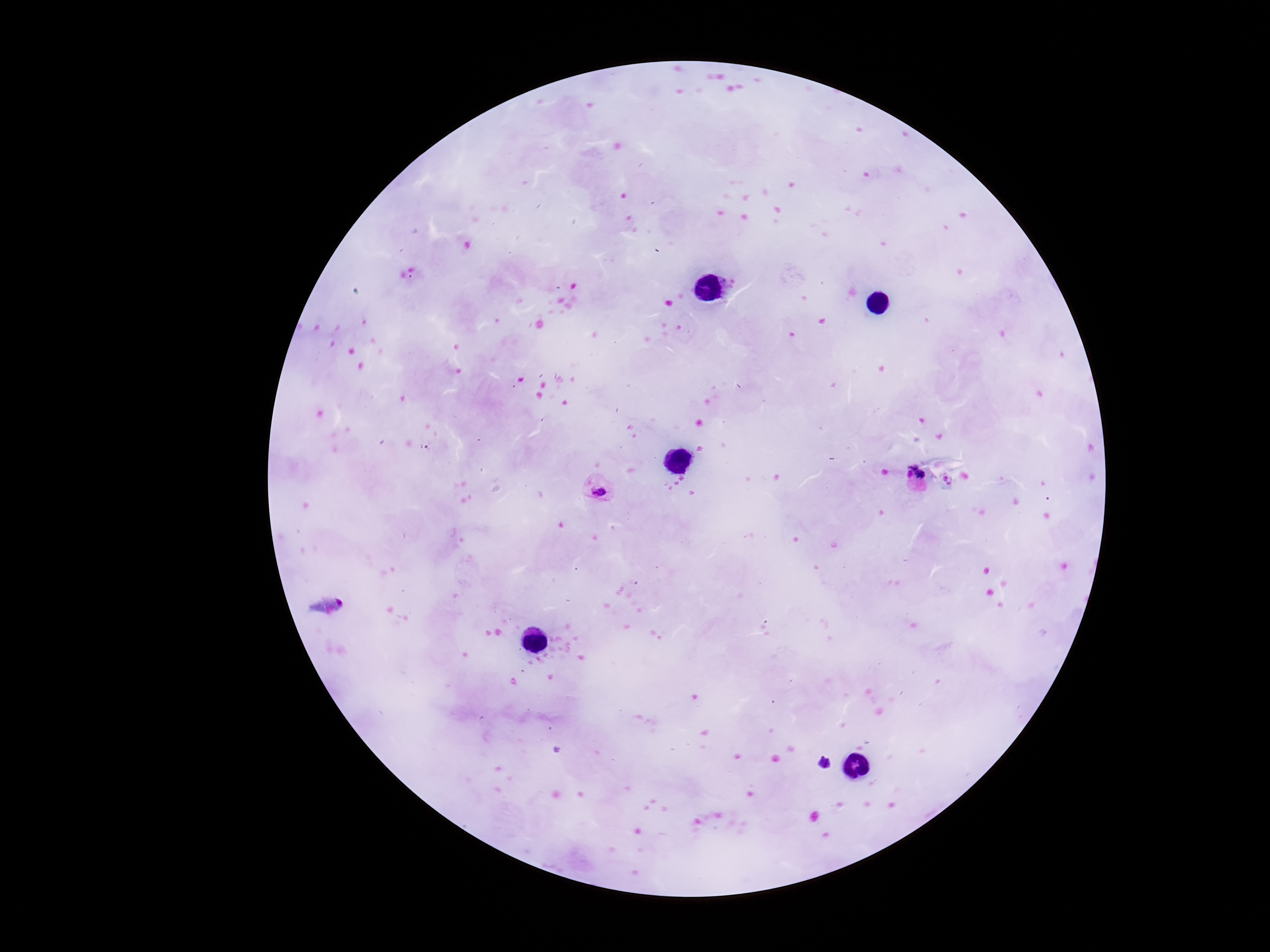 Approximate centers as (x, y) in pixels. Plasmodium parasite locations: (914, 468), (909, 475), (921, 475), (598, 488), (824, 762). Thick blood smear. Giemsa-stained preparation. Single field of view. Patient malaria status: positive. 100x magnification. Image is 1270×952 pixels. Photographed through the microscope eyepiece with a smartphone camera.